Give the position of every malaria parasite.
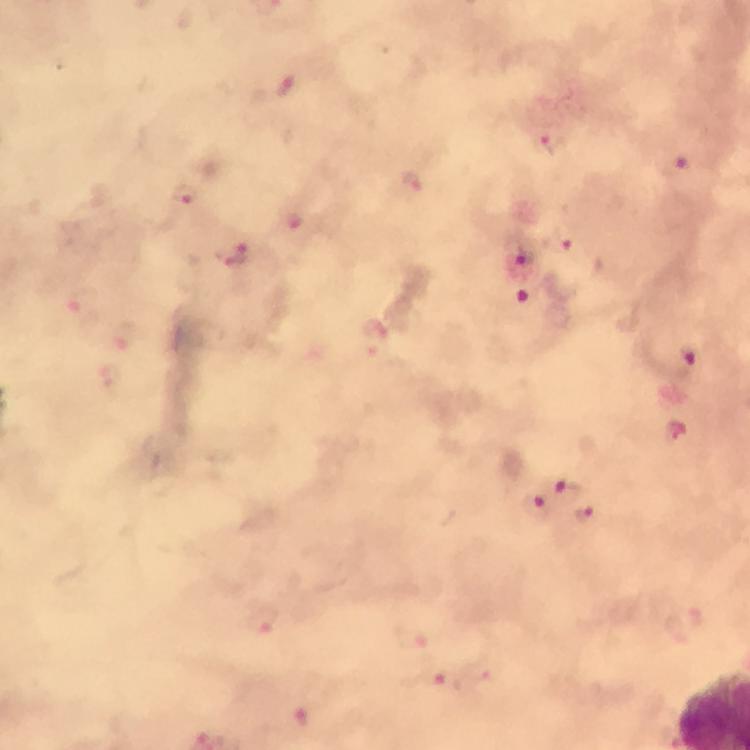
Approximate object centers, in pixels from the top-left corner.
Malaria parasites: (x=287, y=91), (x=548, y=140), (x=677, y=168), (x=413, y=184), (x=184, y=195), (x=567, y=241), (x=525, y=255), (x=233, y=256), (x=529, y=295), (x=684, y=360), (x=566, y=492), (x=536, y=504), (x=586, y=513), (x=259, y=621), (x=412, y=636), (x=433, y=676), (x=300, y=717).

{
  "immersion_oil": "used",
  "magnification": "100x",
  "cropped_from": "a single field of view",
  "stain": "Giemsa",
  "preparation": "thick blood film",
  "image_size": "750×750 pixels",
  "context": "from a diagnostic examination for malaria",
  "capture": "smartphone mounted on the microscope"
}